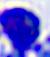

{
  "modality": "photomicrograph",
  "magnification": "400x",
  "identification": "white blood cell"
}